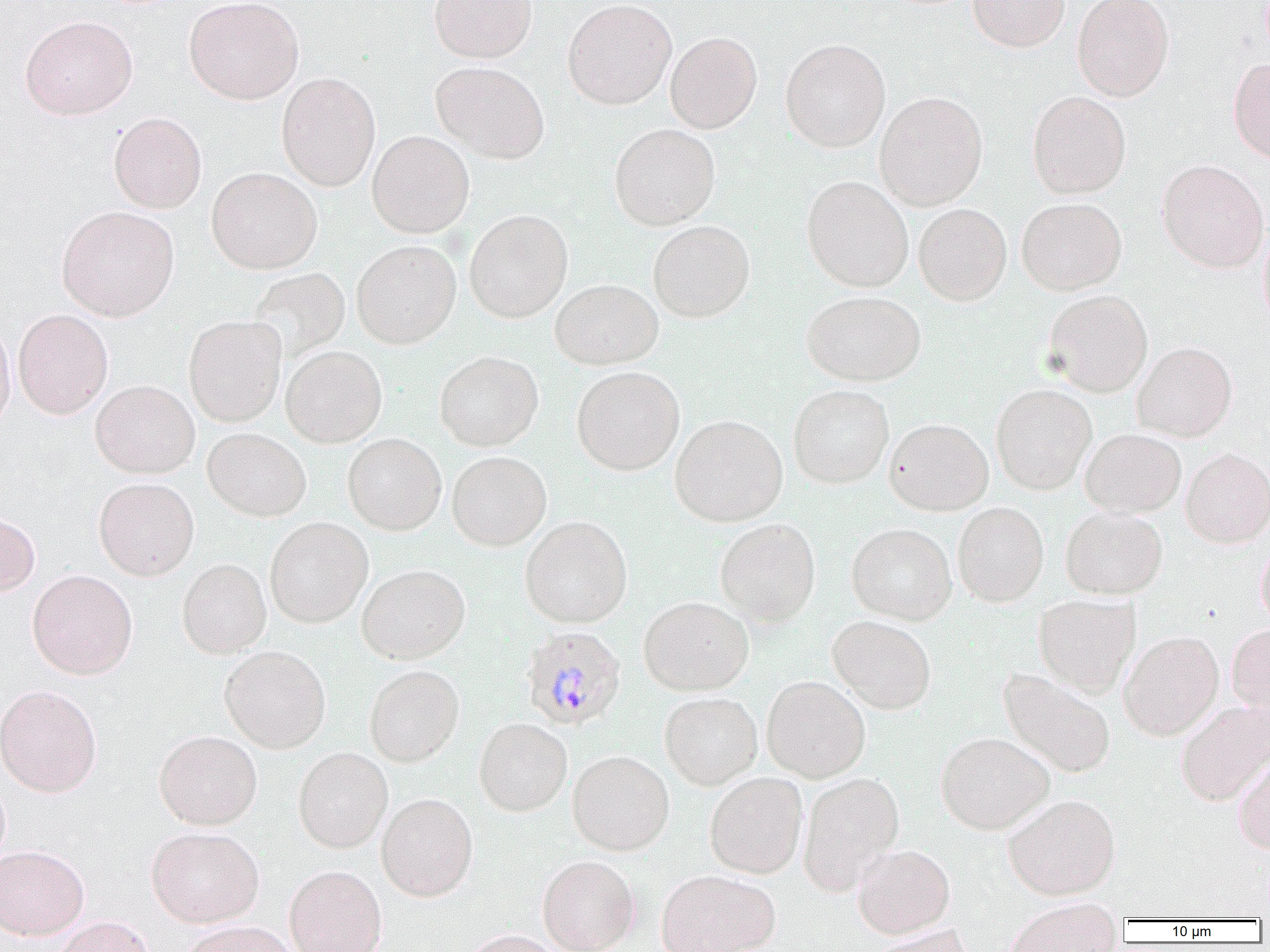

{
  "slide_level_diagnosis": "Plasmodium malariae",
  "uninfected_red_blood_cell_locations": "approximate bounding boxes as [x1, y1, x2, y2] in pixels: [183, 0, 304, 105], [429, 0, 537, 63], [562, 0, 677, 110], [967, 0, 1070, 52], [1072, 0, 1174, 101], [19, 15, 138, 120], [665, 31, 763, 134], [781, 38, 891, 152], [1228, 58, 1270, 163], [430, 61, 550, 163], [276, 72, 381, 192], [874, 91, 988, 211], [1027, 91, 1131, 198], [108, 112, 207, 213], [609, 124, 720, 230], [367, 130, 474, 238], [1157, 159, 1269, 273], [206, 166, 323, 274], [801, 176, 914, 292], [1016, 197, 1127, 295], [913, 203, 1012, 305], [56, 205, 179, 321], [464, 209, 573, 323], [647, 220, 755, 322], [1257, 224, 1270, 333], [351, 239, 461, 349], [247, 267, 351, 363], [550, 278, 664, 370], [801, 290, 926, 387], [1043, 290, 1153, 397], [12, 309, 113, 419], [183, 315, 286, 427], [0, 319, 15, 433], [1133, 341, 1237, 442], [281, 345, 387, 447], [435, 351, 544, 451], [572, 366, 685, 475], [90, 380, 200, 478], [788, 384, 894, 489], [991, 384, 1097, 495], [669, 414, 788, 526], [884, 418, 994, 515], [203, 427, 311, 521], [1080, 428, 1186, 517], [342, 433, 447, 535], [1181, 448, 1270, 547], [447, 451, 551, 551], [93, 477, 199, 580], [953, 502, 1049, 607], [1061, 507, 1167, 599], [0, 512, 40, 596], [520, 516, 633, 628], [265, 517, 373, 628], [715, 518, 821, 625], [846, 522, 957, 625], [1256, 538, 1270, 630], [177, 558, 272, 658], [357, 564, 470, 664], [27, 569, 137, 679], [1034, 594, 1140, 696], [638, 596, 754, 695], [827, 615, 936, 714], [1227, 622, 1270, 717], [1119, 630, 1224, 740], [219, 645, 331, 752], [364, 664, 465, 767], [997, 667, 1117, 778], [761, 675, 870, 782], [0, 684, 102, 797], [659, 691, 763, 790], [1176, 700, 1270, 805], [474, 717, 572, 816], [154, 729, 263, 830], [936, 731, 1054, 834], [293, 747, 392, 853], [567, 749, 675, 855], [1233, 754, 1270, 853], [798, 771, 904, 895], [705, 772, 808, 878], [0, 774, 10, 870], [376, 792, 478, 901], [1003, 794, 1121, 900], [146, 826, 264, 927], [852, 843, 955, 938], [0, 844, 89, 940], [538, 854, 640, 952], [285, 864, 388, 952], [655, 869, 780, 952], [1002, 902, 1122, 952], [51, 915, 155, 952], [179, 920, 298, 952], [867, 925, 976, 952], [460, 929, 572, 952]",
  "plasmodium_malariae_infected_red_blood_cell_locations": "approximate bounding boxes as [x1, y1, x2, y2] in pixels: [521, 625, 626, 730]",
  "field_of_view": "single",
  "preparation": "thin blood smear",
  "modality": "optical microscopy",
  "magnification": "1000x",
  "image_size": "1270×952 pixels"
}